Comment on the morphology of the red blood cells.
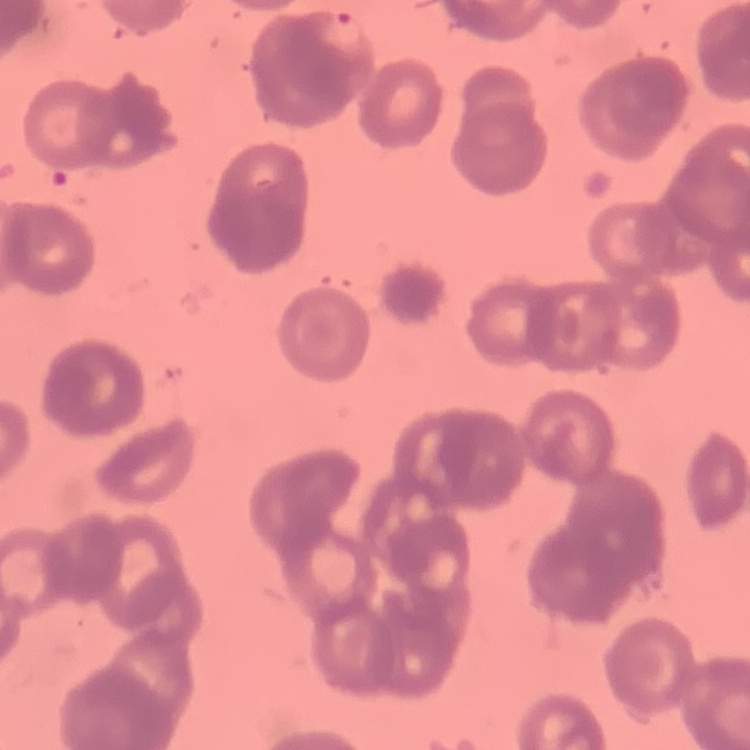
Rouleaux formation.

{
  "image_type": "one tile cut from a larger photomicrograph",
  "stain": "Field's or Giemsa",
  "preparation": "thin blood smear"
}